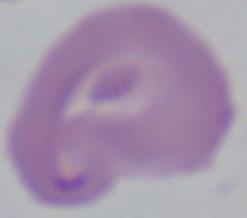

Captured at 1000x magnification. A Babesia parasite is seen. Photomicrograph.